Assess this cell for malaria.
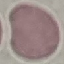

Uninfected.

Summary:
  - Stain: Giemsa
  - Capture: smartphone camera at the microscope eyepiece
  - Preparation: thin blood film
  - Image type: automatically extracted cell patch, resized to 64 × 64 pixels